Classify this cell by malaria status.
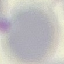
It is uninfected.

Giemsa-stained preparation. Automatically extracted cell patch, resized to 64 × 64 pixels. Thin smear of blood. Acquired by smartphone through the microscope eyepiece.